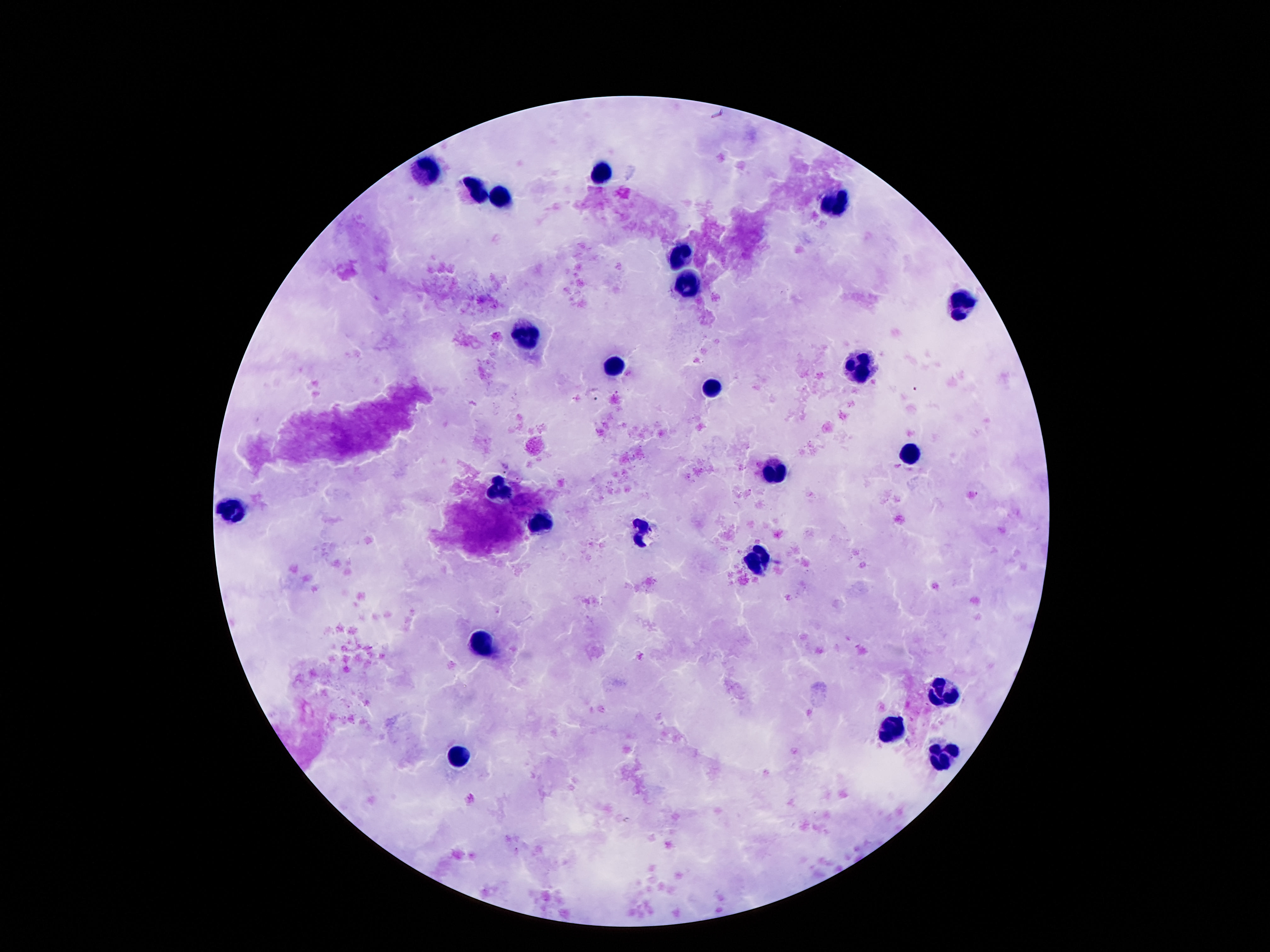
{
  "capture": "smartphone camera through the microscope eyepiece",
  "patient_malaria_status": "not infected",
  "magnification": "100x",
  "preparation": "thick blood film",
  "image_size": "1270×952 pixels",
  "leukocyte_locations": "approximate centers as (x, y) in pixels: (426, 172), (605, 172), (481, 189), (501, 196), (833, 201), (680, 254), (693, 282), (961, 302), (527, 335), (614, 367), (863, 367), (715, 388), (910, 453), (775, 471), (499, 486), (231, 508), (541, 524), (642, 530), (760, 561), (479, 645), (943, 689), (892, 724), (457, 756), (941, 758)",
  "field_of_view": "single",
  "stain": "Giemsa"
}